State which parasite is depicted.
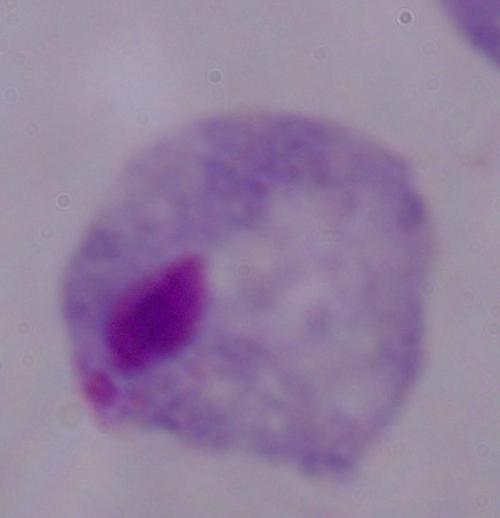
A trichomonad.

modality: micrograph
magnification: 1000x